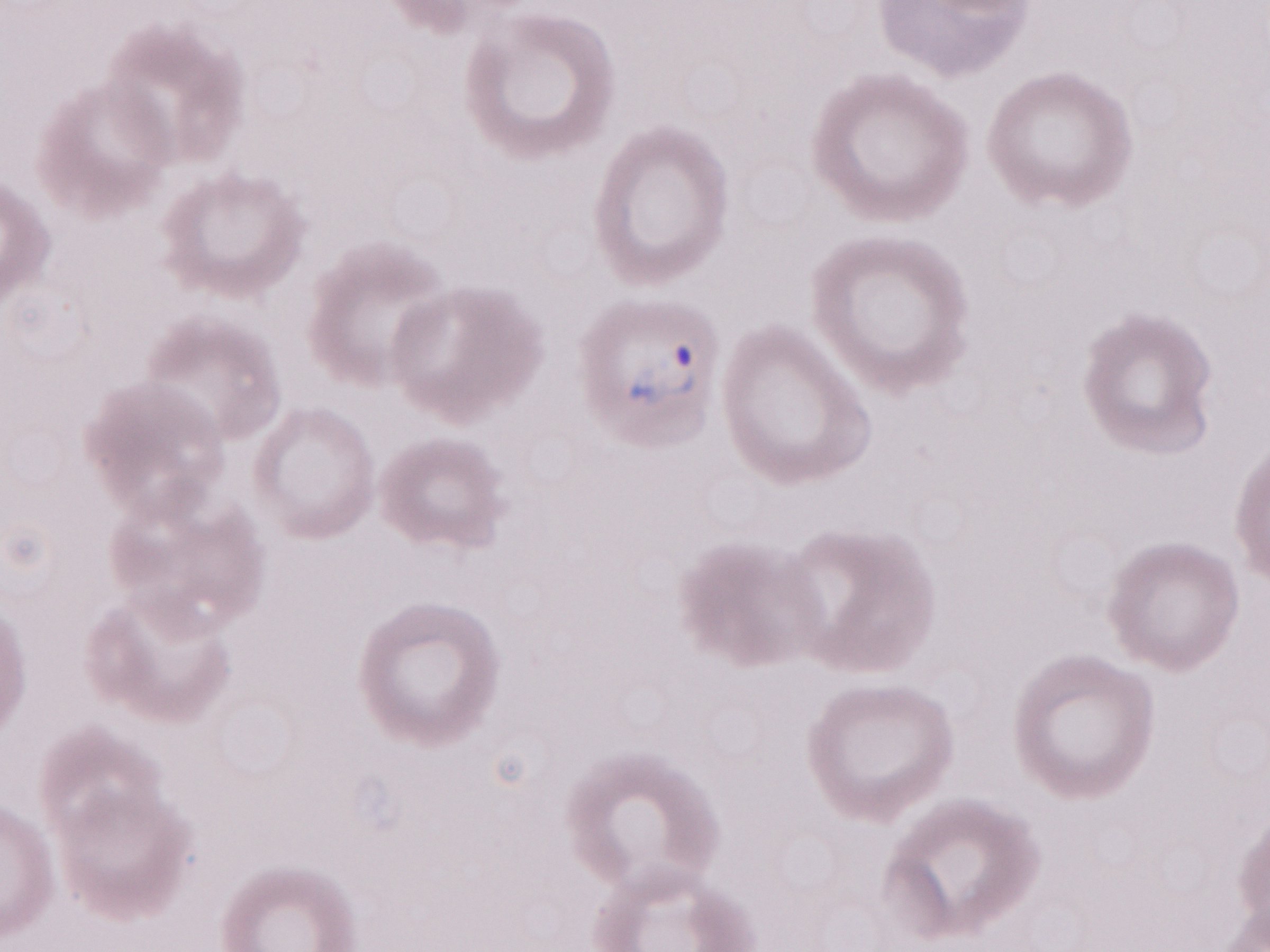 Olympus BX43 microscope and DP73 digital camera. Magnification: 1,000x. May-Grünwald-Giemsa stain. Patient-level malaria diagnosis: positive. Thin peripheral-blood smear. Single field of view. Image is 1270×952 pixels.